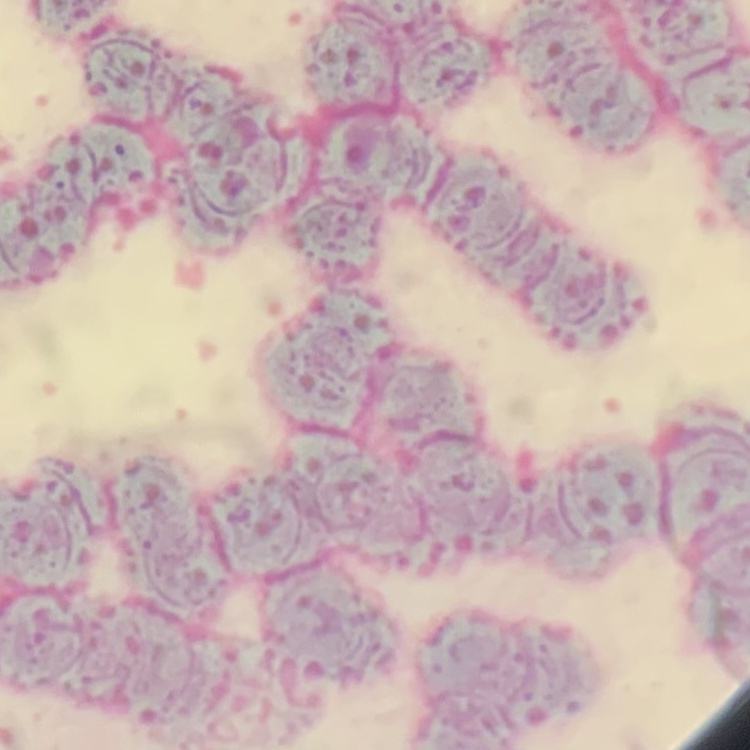
{
  "erythrocyte_morphology": "rouleaux formation",
  "preparation": "thin blood smear",
  "image_type": "square crop of a larger photomicrograph",
  "stain": "Field's or Giemsa"
}